Assess this cell for malaria.
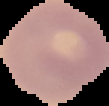

It is uninfected.

Summary:
  - Image size: 109×106 pixels
  - Preparation: thin blood smear
  - Image type: segmented cell region with the area outside set to black